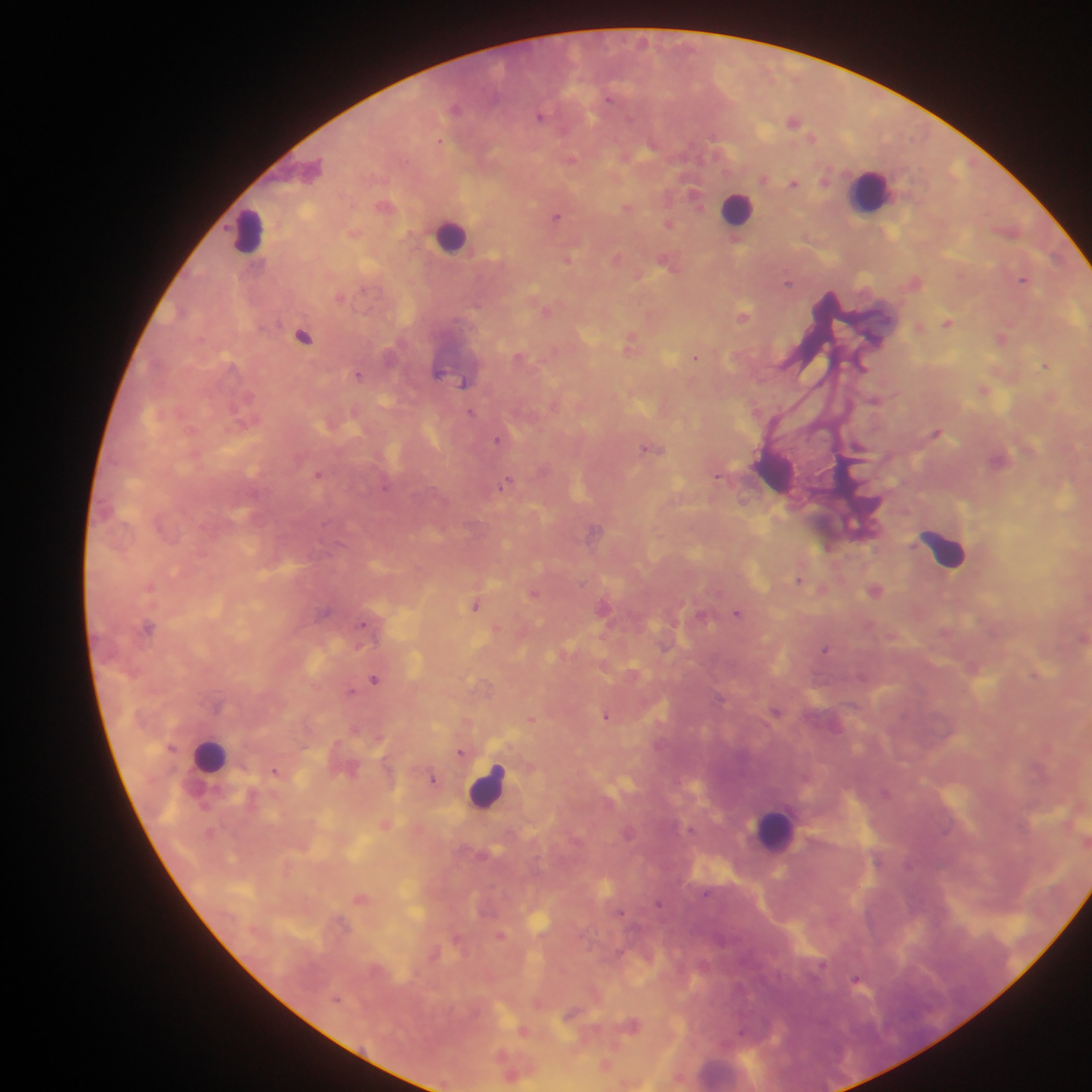

leukocyte_locations: 'approximate centers as (x, y) in pixels: (870, 189), (737, 208), (249, 231), (451, 236), (774, 469), (944, 549), (210, 756), (487, 786), (775, 830)'
country: Ghana
field_of_view: single
plasmodium_parasite_locations: 'approximate centers as (x, y) in pixels: (455, 108), (541, 116), (794, 119), (441, 140), (571, 159), (794, 182), (695, 193), (386, 205), (628, 207), (557, 216), (669, 223), (618, 257), (568, 259), (670, 262), (1023, 279), (915, 281), (788, 283), (341, 296), (546, 309), (744, 315), (947, 322), (920, 326), (303, 336), (1002, 338), (632, 343), (695, 357), (522, 358), (1045, 365), (358, 374), (465, 383), (984, 388), (472, 412), (936, 431), (500, 439), (652, 448), (318, 473), (719, 475), (507, 482), (743, 501), (594, 531), (799, 580), (151, 586), (822, 589), (876, 589), (534, 593), (476, 605), (605, 606), (738, 612), (366, 625), (148, 626), (498, 629), (1082, 638), (826, 649), (375, 678), (351, 691), (777, 711), (607, 716), (532, 719), (461, 753), (275, 770), (433, 779), (385, 823), (361, 898), (659, 903), (501, 935), (458, 939), (434, 953), (822, 965), (858, 980), (572, 1012), (633, 1024), (524, 1030), (606, 1064), (512, 1074)'
preparation: thick blood smear
image_size: 1092×1092 pixels
capture: mobile-phone photograph through a microscope